Assess this cell for malaria.
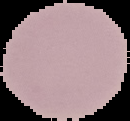
It is uninfected.

preparation = thin blood film
image type = cell region segmented out of the field of view; surrounding area masked to black
image size = 130×121 pixels